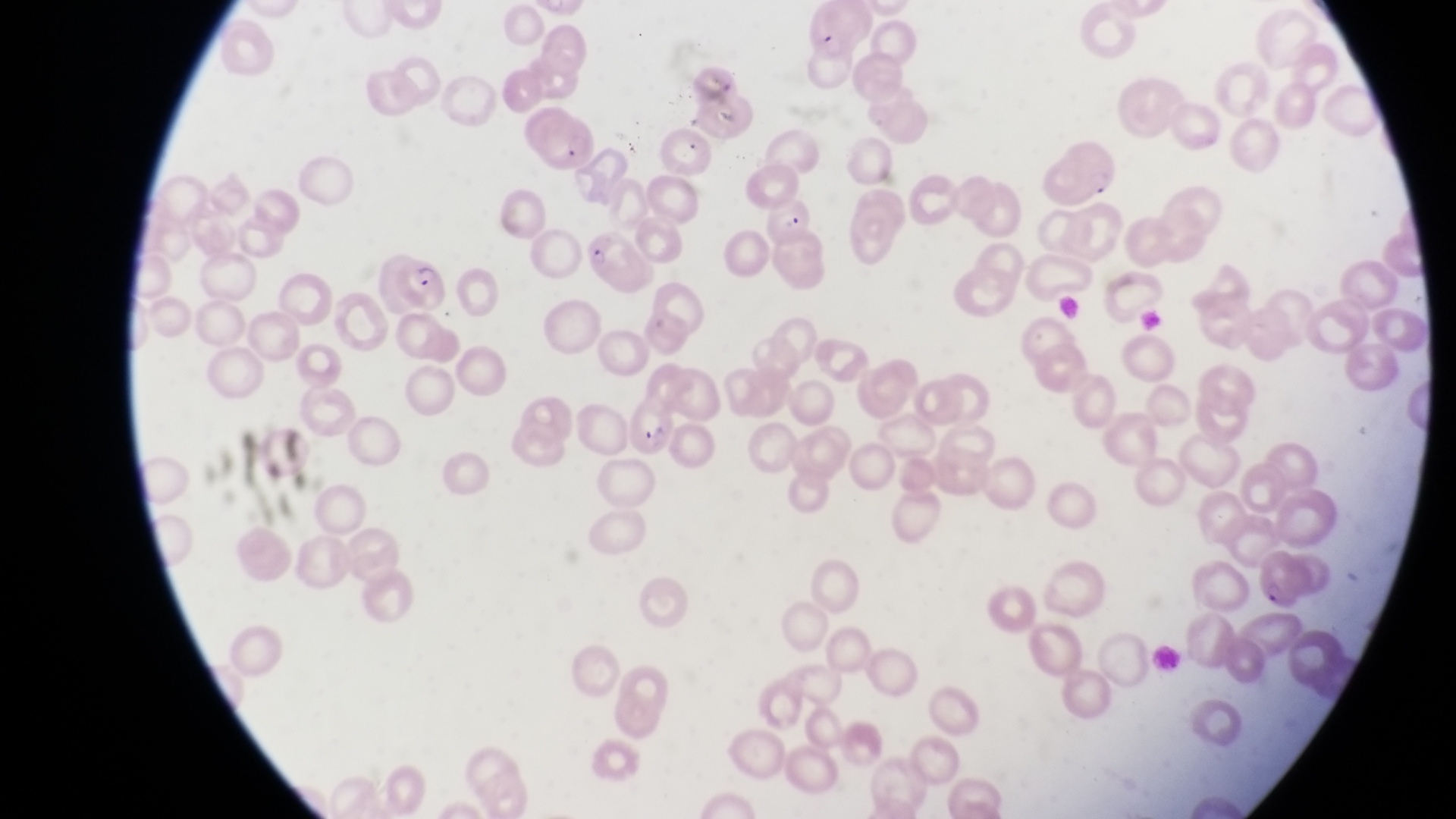 Approximate bounding boxes as (left, top, right, bottom) in pixels. Parasitised red blood cell locations: (806, 7, 877, 63), (522, 109, 596, 168), (1067, 132, 1120, 198), (766, 193, 816, 249), (584, 227, 650, 291), (391, 253, 451, 316), (617, 399, 675, 457), (1252, 549, 1304, 608). Artifact (platelet-like body, stain precipitate, or debris) locations: (708, 93, 741, 126). Photographed through the eyepiece of an Olympus CX-23 microscope with a smartphone camera. Image is 1456×819 pixels. Thin blood film. Magnification of 1000x. One field of view. Sample from Uganda.